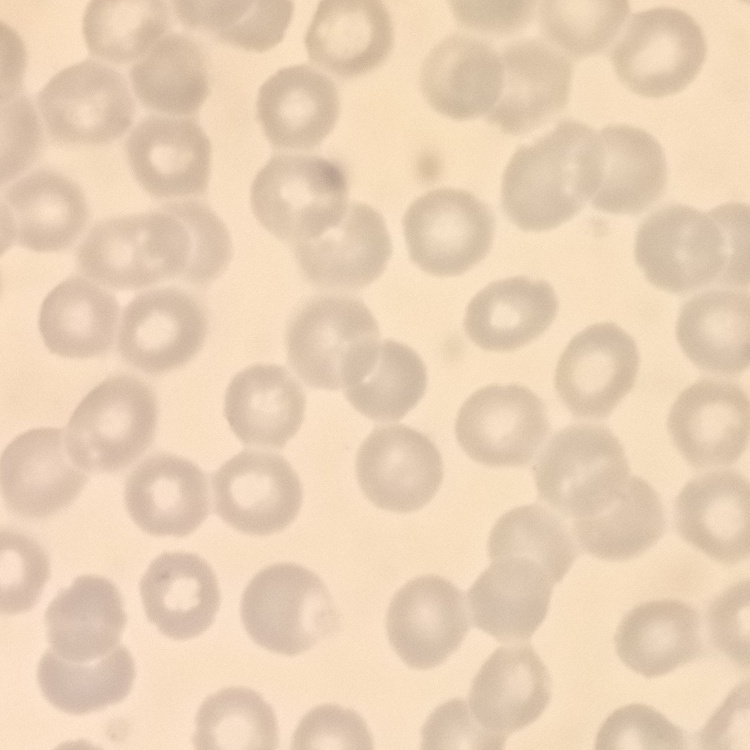

erythrocyte morphology = no rouleaux formation
preparation = thin blood film
image type = one tile cut from a larger photomicrograph
stain = Field's or Giemsa